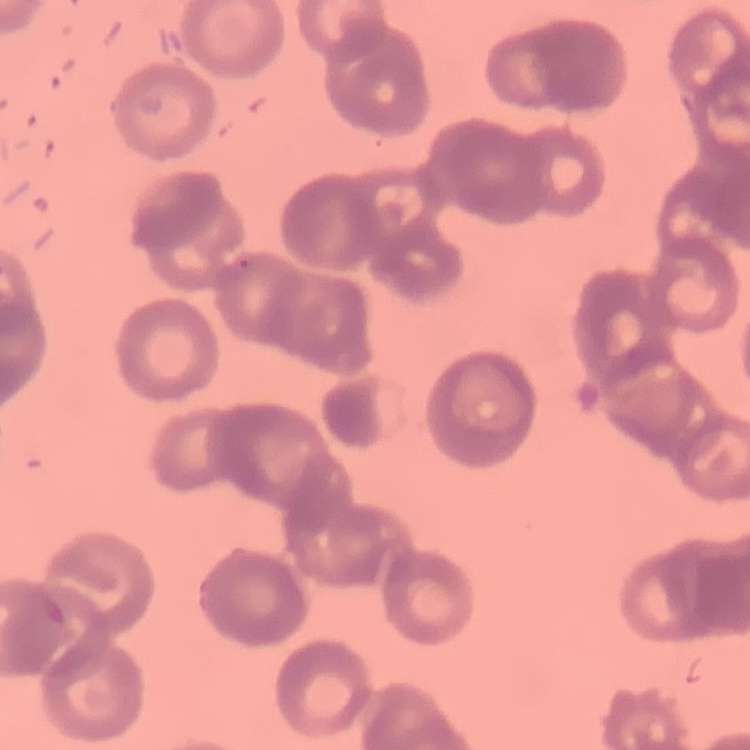

The erythrocytes show rouleaux formation. Thin peripheral smear. Stained with either Field's or Giemsa. One tile cut from a larger photomicrograph.